Classify this cell by malaria status.
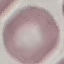
It is uninfected.

Automatically extracted cell patch, resized to 64 × 64 pixels. Photographed with a smartphone camera at the microscope eyepiece. Giemsa-stained preparation. Thin blood smear.